Comment on the morphology of the red blood cells.
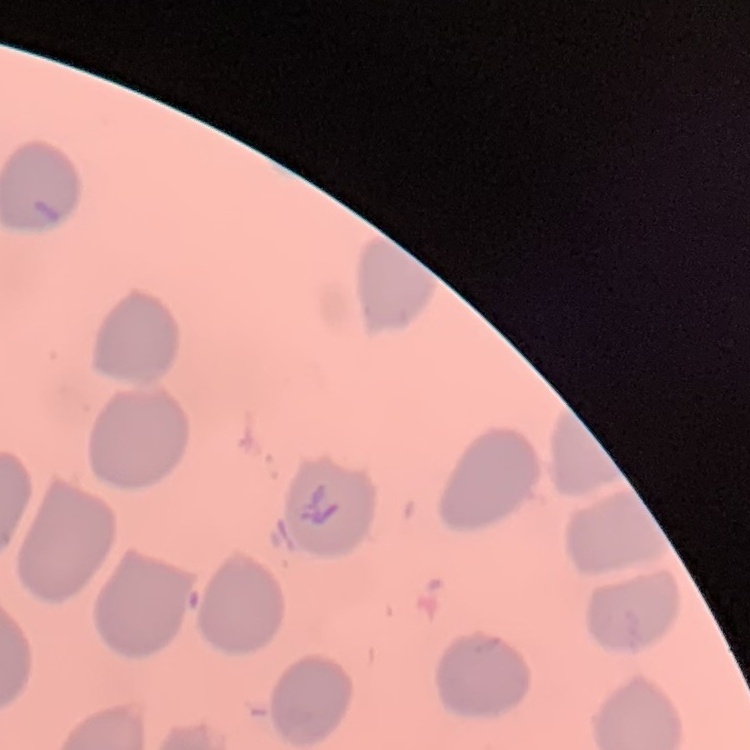

They show no rouleaux formation.

Square crop of a larger photomicrograph. Thin blood smear. Stained with either Field's or Giemsa.